Name the cell type shown.
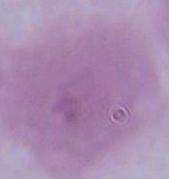
An erythrocyte.

{
  "modality": "micrograph",
  "magnification": "1000x"
}